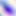
Toxoplasma gondii is seen. Micrograph. 400x magnification.